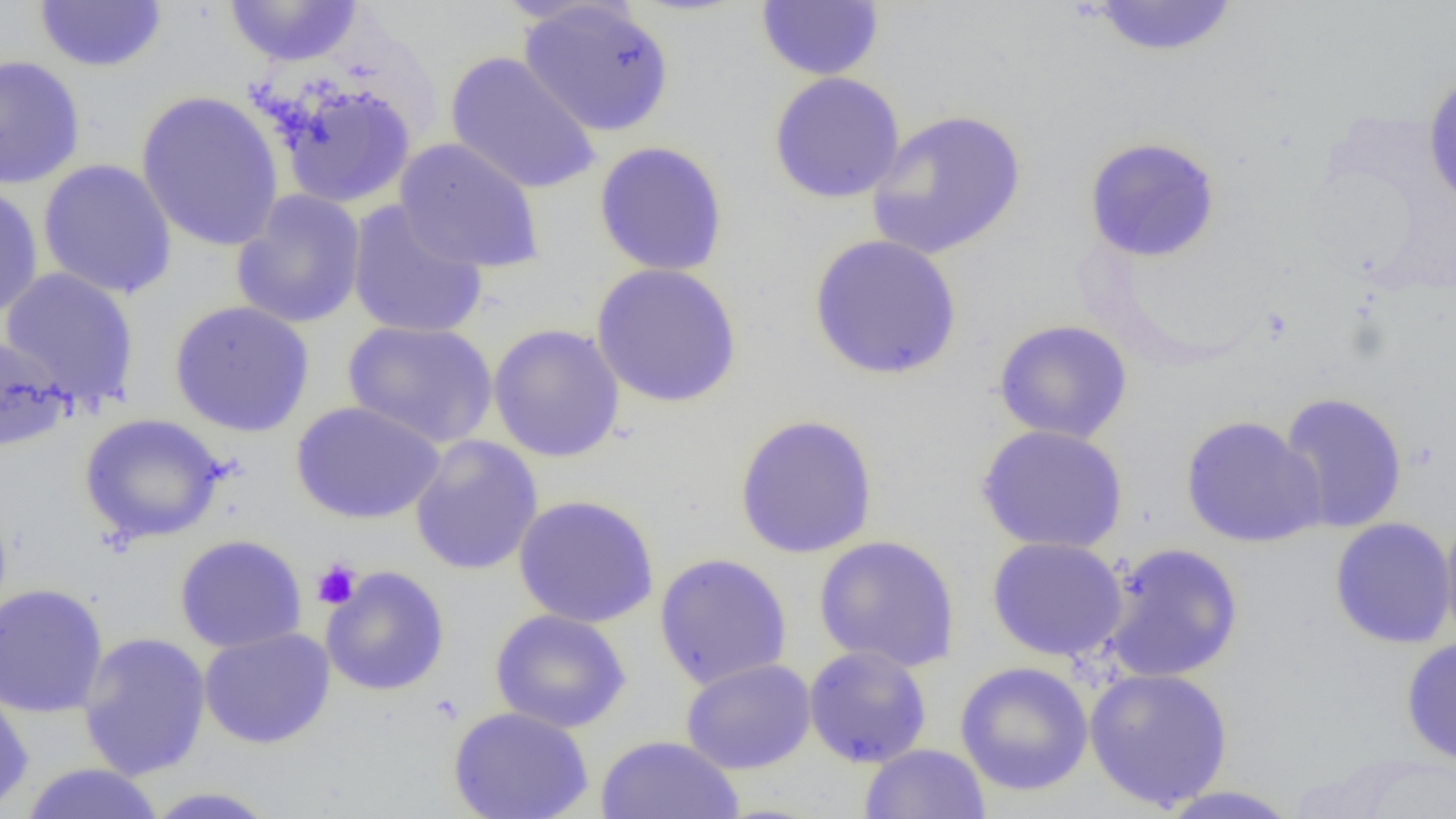
slide-level diagnosis = negative for blood parasites
modality = optical microscopy
magnification = 1000x
preparation = thin blood film
image size = 1456×819 pixels
uninfected red blood cell locations = approximate bounding boxes as named x1/y1/x2/y2 corners in pixels: (x1=223, y1=0, x2=364, y2=67), (x1=1084, y1=0, x2=1240, y2=59), (x1=34, y1=1, x2=167, y2=72), (x1=517, y1=1, x2=676, y2=138), (x1=755, y1=1, x2=885, y2=81), (x1=445, y1=52, x2=602, y2=195), (x1=0, y1=54, x2=85, y2=190), (x1=768, y1=71, x2=906, y2=204), (x1=1421, y1=71, x2=1456, y2=212), (x1=269, y1=79, x2=418, y2=210), (x1=135, y1=90, x2=286, y2=252), (x1=866, y1=108, x2=1027, y2=261), (x1=1083, y1=135, x2=1222, y2=263), (x1=394, y1=138, x2=545, y2=274), (x1=593, y1=141, x2=729, y2=277), (x1=38, y1=158, x2=178, y2=301), (x1=0, y1=184, x2=44, y2=319), (x1=231, y1=189, x2=367, y2=329), (x1=346, y1=200, x2=488, y2=340), (x1=808, y1=233, x2=963, y2=381), (x1=591, y1=262, x2=743, y2=408), (x1=0, y1=267, x2=140, y2=409), (x1=168, y1=300, x2=315, y2=437), (x1=993, y1=319, x2=1133, y2=444), (x1=343, y1=320, x2=498, y2=448), (x1=487, y1=322, x2=626, y2=464), (x1=0, y1=334, x2=74, y2=454), (x1=1277, y1=391, x2=1408, y2=534), (x1=290, y1=401, x2=446, y2=525), (x1=78, y1=413, x2=228, y2=545), (x1=734, y1=413, x2=878, y2=559), (x1=1179, y1=415, x2=1326, y2=548), (x1=975, y1=424, x2=1129, y2=554), (x1=408, y1=435, x2=543, y2=575), (x1=513, y1=494, x2=660, y2=628), (x1=1439, y1=508, x2=1456, y2=652), (x1=1329, y1=517, x2=1455, y2=649), (x1=173, y1=534, x2=308, y2=653), (x1=812, y1=534, x2=961, y2=673), (x1=986, y1=536, x2=1128, y2=663), (x1=1100, y1=542, x2=1244, y2=683), (x1=653, y1=552, x2=792, y2=690), (x1=320, y1=566, x2=450, y2=696), (x1=0, y1=583, x2=109, y2=718), (x1=490, y1=609, x2=631, y2=733), (x1=198, y1=627, x2=336, y2=749), (x1=77, y1=631, x2=211, y2=781), (x1=1400, y1=635, x2=1456, y2=767), (x1=803, y1=645, x2=933, y2=768), (x1=680, y1=657, x2=817, y2=775), (x1=954, y1=661, x2=1094, y2=796), (x1=1084, y1=666, x2=1233, y2=811), (x1=0, y1=685, x2=34, y2=813), (x1=448, y1=706, x2=594, y2=819), (x1=595, y1=734, x2=744, y2=819), (x1=859, y1=743, x2=991, y2=819), (x1=20, y1=762, x2=167, y2=819), (x1=1153, y1=785, x2=1305, y2=818), (x1=141, y1=786, x2=281, y2=818)
platelet locations = approximate bounding boxes as named x1/y1/x2/y2 corners in pixels: (x1=312, y1=558, x2=362, y2=609)
field of view = single